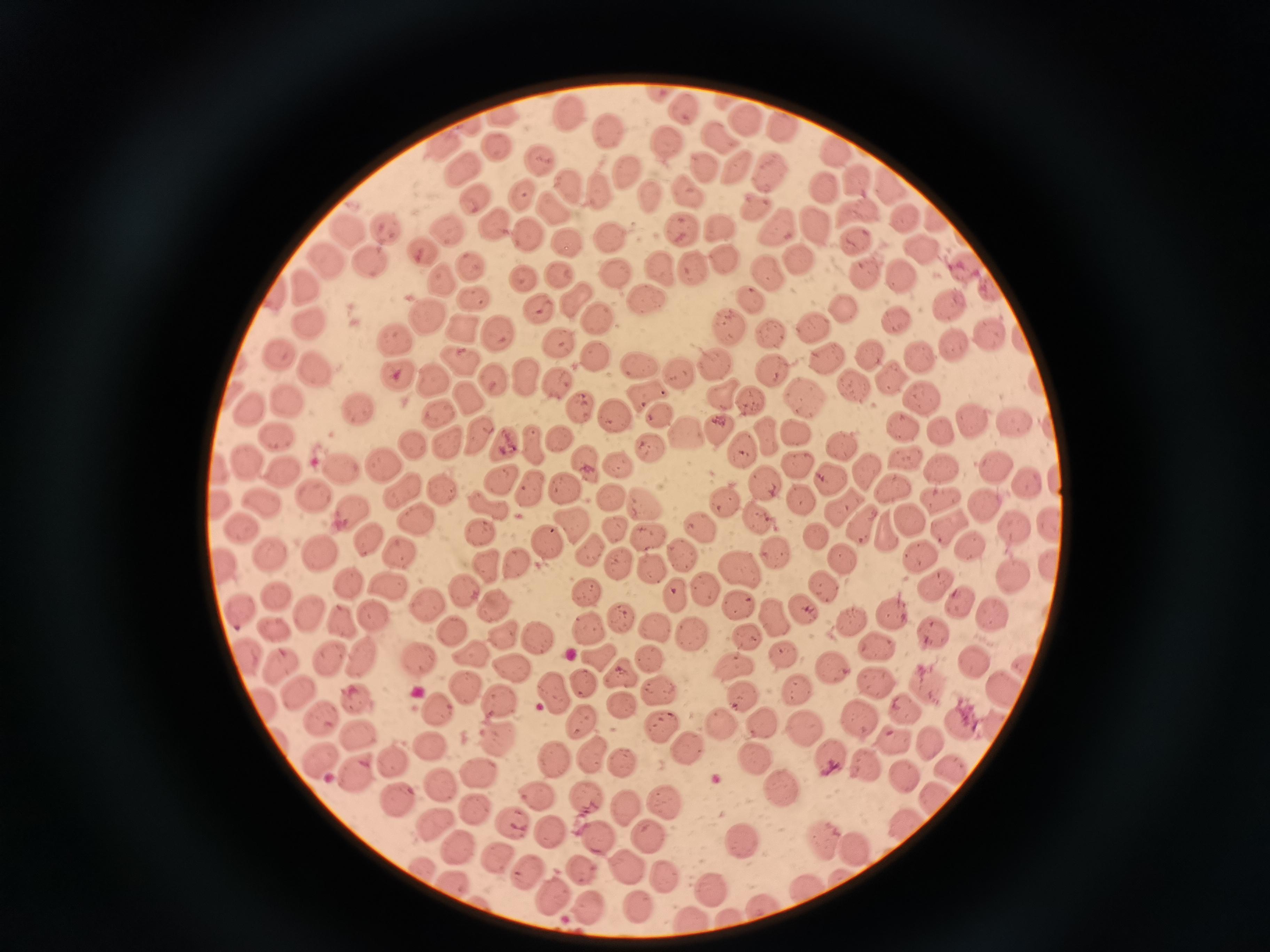
Approximate object centers, in pixels from the top-left corner.
Summary:
  - Cell locations: (x=663, y=93), (x=688, y=109), (x=507, y=113), (x=569, y=113), (x=744, y=117), (x=781, y=125), (x=609, y=134), (x=721, y=137), (x=666, y=143), (x=493, y=144), (x=450, y=145), (x=834, y=150), (x=543, y=158), (x=701, y=168), (x=467, y=170), (x=742, y=171), (x=773, y=173), (x=626, y=174), (x=855, y=180), (x=889, y=181), (x=823, y=185), (x=687, y=188), (x=573, y=189), (x=522, y=194), (x=604, y=194), (x=649, y=195), (x=477, y=196), (x=754, y=206), (x=556, y=210), (x=858, y=212), (x=934, y=213), (x=906, y=218), (x=489, y=223), (x=781, y=226), (x=812, y=226), (x=354, y=229), (x=384, y=230), (x=684, y=230), (x=530, y=232), (x=448, y=233), (x=610, y=234), (x=852, y=240), (x=570, y=243), (x=419, y=248), (x=920, y=248), (x=799, y=261), (x=335, y=263), (x=471, y=263), (x=371, y=264), (x=664, y=267), (x=964, y=269), (x=696, y=270), (x=616, y=271), (x=768, y=274), (x=870, y=274), (x=561, y=275), (x=905, y=275), (x=524, y=279), (x=445, y=282), (x=310, y=288), (x=989, y=288), (x=474, y=298), (x=649, y=298), (x=752, y=298), (x=946, y=301), (x=584, y=302), (x=541, y=306), (x=844, y=307), (x=427, y=315), (x=604, y=318), (x=893, y=320), (x=314, y=323), (x=811, y=324), (x=729, y=327), (x=461, y=330), (x=772, y=331), (x=498, y=334), (x=992, y=335), (x=397, y=338), (x=558, y=340), (x=949, y=343), (x=279, y=351), (x=915, y=352), (x=866, y=354), (x=827, y=355), (x=593, y=356), (x=462, y=361), (x=318, y=362), (x=636, y=362), (x=715, y=363), (x=682, y=370), (x=777, y=373), (x=399, y=374), (x=529, y=376), (x=433, y=378), (x=493, y=380), (x=887, y=380), (x=563, y=382), (x=851, y=385), (x=724, y=392), (x=805, y=393), (x=469, y=394), (x=649, y=394), (x=922, y=396), (x=287, y=401), (x=748, y=403), (x=248, y=405), (x=583, y=409), (x=359, y=412), (x=441, y=414), (x=614, y=415), (x=662, y=418), (x=1013, y=420), (x=970, y=421), (x=908, y=424), (x=719, y=425), (x=943, y=432), (x=279, y=433), (x=688, y=434), (x=481, y=436), (x=796, y=436), (x=533, y=437), (x=764, y=437), (x=561, y=440), (x=415, y=443), (x=843, y=443), (x=448, y=445), (x=504, y=445), (x=650, y=449), (x=741, y=450), (x=905, y=456), (x=247, y=459), (x=382, y=460), (x=800, y=462), (x=588, y=463), (x=620, y=465), (x=942, y=466), (x=342, y=468), (x=865, y=468), (x=993, y=468), (x=285, y=472), (x=498, y=475), (x=763, y=478), (x=830, y=478), (x=1030, y=485), (x=562, y=486), (x=403, y=487), (x=529, y=487), (x=895, y=488), (x=441, y=490), (x=315, y=491), (x=611, y=492), (x=726, y=496), (x=804, y=499), (x=262, y=500), (x=641, y=500), (x=937, y=500), (x=493, y=506), (x=986, y=508), (x=349, y=509), (x=853, y=515), (x=912, y=520), (x=755, y=522), (x=423, y=524), (x=565, y=524), (x=1015, y=524), (x=700, y=525), (x=947, y=525), (x=246, y=528), (x=615, y=528), (x=481, y=533), (x=649, y=533), (x=819, y=535), (x=368, y=538), (x=548, y=545), (x=971, y=545), (x=922, y=548), (x=322, y=549), (x=592, y=550), (x=679, y=550), (x=401, y=551), (x=273, y=552), (x=776, y=554), (x=847, y=555), (x=224, y=560), (x=486, y=561), (x=523, y=562), (x=620, y=566), (x=653, y=566), (x=742, y=567), (x=1011, y=575), (x=346, y=581), (x=935, y=582), (x=824, y=585), (x=388, y=586), (x=467, y=587), (x=704, y=587), (x=586, y=588), (x=677, y=596), (x=278, y=597), (x=959, y=600), (x=426, y=603), (x=738, y=605), (x=498, y=606), (x=804, y=609), (x=241, y=611), (x=893, y=611), (x=622, y=613), (x=989, y=614), (x=775, y=615), (x=308, y=616), (x=849, y=618), (x=375, y=621), (x=591, y=623), (x=348, y=624), (x=656, y=626), (x=451, y=628), (x=272, y=629), (x=934, y=631), (x=748, y=634), (x=537, y=636), (x=505, y=639), (x=692, y=639), (x=878, y=645), (x=787, y=653), (x=475, y=654), (x=249, y=655), (x=599, y=655), (x=653, y=655), (x=338, y=659), (x=975, y=659), (x=361, y=660), (x=419, y=660), (x=282, y=662), (x=735, y=664), (x=830, y=665), (x=514, y=668), (x=621, y=676), (x=876, y=680), (x=929, y=681), (x=584, y=684), (x=469, y=687), (x=801, y=687), (x=560, y=688), (x=1005, y=688), (x=658, y=693), (x=745, y=693), (x=302, y=697), (x=503, y=698), (x=359, y=702), (x=435, y=705), (x=622, y=706), (x=267, y=708), (x=906, y=708), (x=326, y=719), (x=863, y=720), (x=965, y=720), (x=584, y=722), (x=726, y=724), (x=761, y=724), (x=661, y=725), (x=805, y=726), (x=995, y=726), (x=357, y=733), (x=496, y=733), (x=895, y=738), (x=932, y=743), (x=430, y=746), (x=690, y=747), (x=595, y=753), (x=829, y=753), (x=553, y=756), (x=393, y=761), (x=862, y=762), (x=626, y=763), (x=757, y=763), (x=955, y=768), (x=354, y=771), (x=481, y=772), (x=899, y=772), (x=444, y=784), (x=784, y=789), (x=537, y=790), (x=397, y=798), (x=586, y=798), (x=666, y=801), (x=476, y=807), (x=626, y=807), (x=905, y=818), (x=431, y=820), (x=512, y=823), (x=551, y=827), (x=598, y=834), (x=824, y=834), (x=646, y=835), (x=458, y=839), (x=740, y=839), (x=849, y=840), (x=501, y=858), (x=629, y=863), (x=587, y=867), (x=528, y=869), (x=665, y=877), (x=456, y=882), (x=711, y=887), (x=808, y=890), (x=558, y=896), (x=650, y=902), (x=592, y=906), (x=766, y=907), (x=734, y=919), (x=696, y=922)
  - Image size: 1270×952 pixels
  - Preparation: thin blood film
  - Field of view: single
  - Capture: smartphone camera at the microscope eyepiece
  - Stain: Giemsa